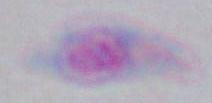
Summary:
  - Modality: micrograph
  - Identification: Toxoplasma gondii
  - Magnification: 1000x